Locate and identify every blood parasite.
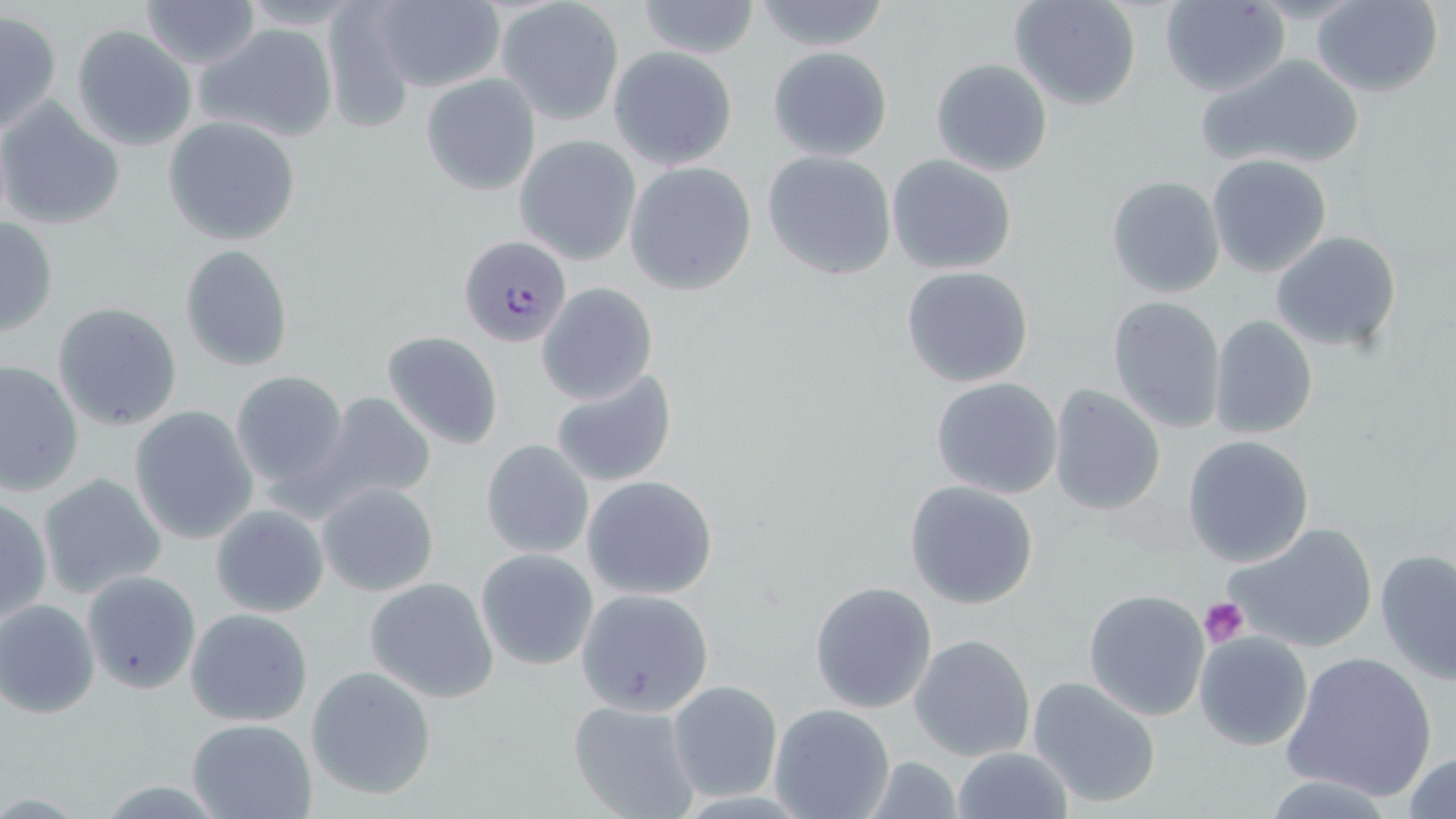
Approximate bounding boxes as (x1,y1)-(x2,y2) corner pairs in pixels.
Plasmodium falciparum-infected red blood cells: (458,234)-(570,347).
No Plasmodium ovale, Plasmodium malariae, Plasmodium vivax, Babesia divergens, or Trypanosoma brucei observed.

slide-level diagnosis = Plasmodium falciparum
uninfected red blood cell locations = approximate bounding boxes as (x1,y1)-(x2,y2) corner pairs in pixels: (140,0)-(260,68), (634,0)-(763,60), (1010,0)-(1142,110), (1159,0)-(1290,98), (1311,0)-(1444,97), (371,1)-(505,94), (749,1)-(894,53), (498,2)-(625,126), (0,11)-(60,134), (196,22)-(339,143), (71,24)-(197,152), (608,46)-(738,170), (766,46)-(893,162), (1198,52)-(1367,173), (930,57)-(1053,176), (421,74)-(541,195), (0,99)-(124,231), (164,116)-(300,245), (514,136)-(641,265), (761,151)-(896,281), (886,154)-(1019,276), (1206,154)-(1333,278), (624,161)-(757,295), (1105,175)-(1225,298), (1,215)-(60,339), (1270,230)-(1402,354), (180,244)-(295,372), (901,265)-(1036,389), (537,283)-(658,404), (1107,295)-(1227,432), (52,302)-(184,431), (1208,314)-(1318,441), (384,331)-(503,449), (0,358)-(84,496), (231,370)-(348,493), (550,370)-(677,487), (930,378)-(1064,499), (1048,384)-(1167,515), (320,393)-(437,508), (129,406)-(258,544), (1183,435)-(1315,567), (480,439)-(596,562), (38,472)-(167,599), (580,476)-(717,600), (904,481)-(1039,609), (317,482)-(439,598), (0,496)-(49,628), (211,503)-(329,618), (1223,521)-(1381,656), (1375,548)-(1456,684), (475,549)-(598,671), (81,571)-(201,694), (364,578)-(499,703), (809,582)-(938,714), (1083,587)-(1213,721), (575,588)-(713,717), (1,599)-(100,717), (184,608)-(314,727), (1193,630)-(1312,751), (909,633)-(1036,761), (1281,650)-(1436,804), (306,666)-(437,800), (1025,674)-(1164,809), (666,681)-(782,801), (568,699)-(703,817), (769,703)-(895,819), (184,717)-(318,819), (950,746)-(1071,819), (1404,752)-(1456,819)
preparation = thin blood film
modality = light microscopy
magnification = 1000x
image size = 1456×819 pixels
stain = May-Grünwald-Giemsa
field of view = one of a larger specimen
platelet locations = approximate bounding boxes as (x1,y1)-(x2,y2) corner pairs in pixels: (1200,596)-(1250,649)